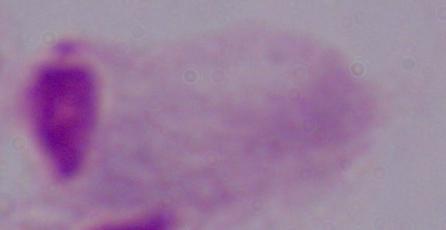
Summary:
  - Magnification: 1000x
  - Modality: micrograph
  - Identification: trichomonad